Report the malaria status of this cell.
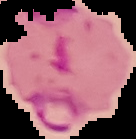
Parasitized.

From a thin blood smear. Segmented cell region on a black background. Image is 136×139 pixels.